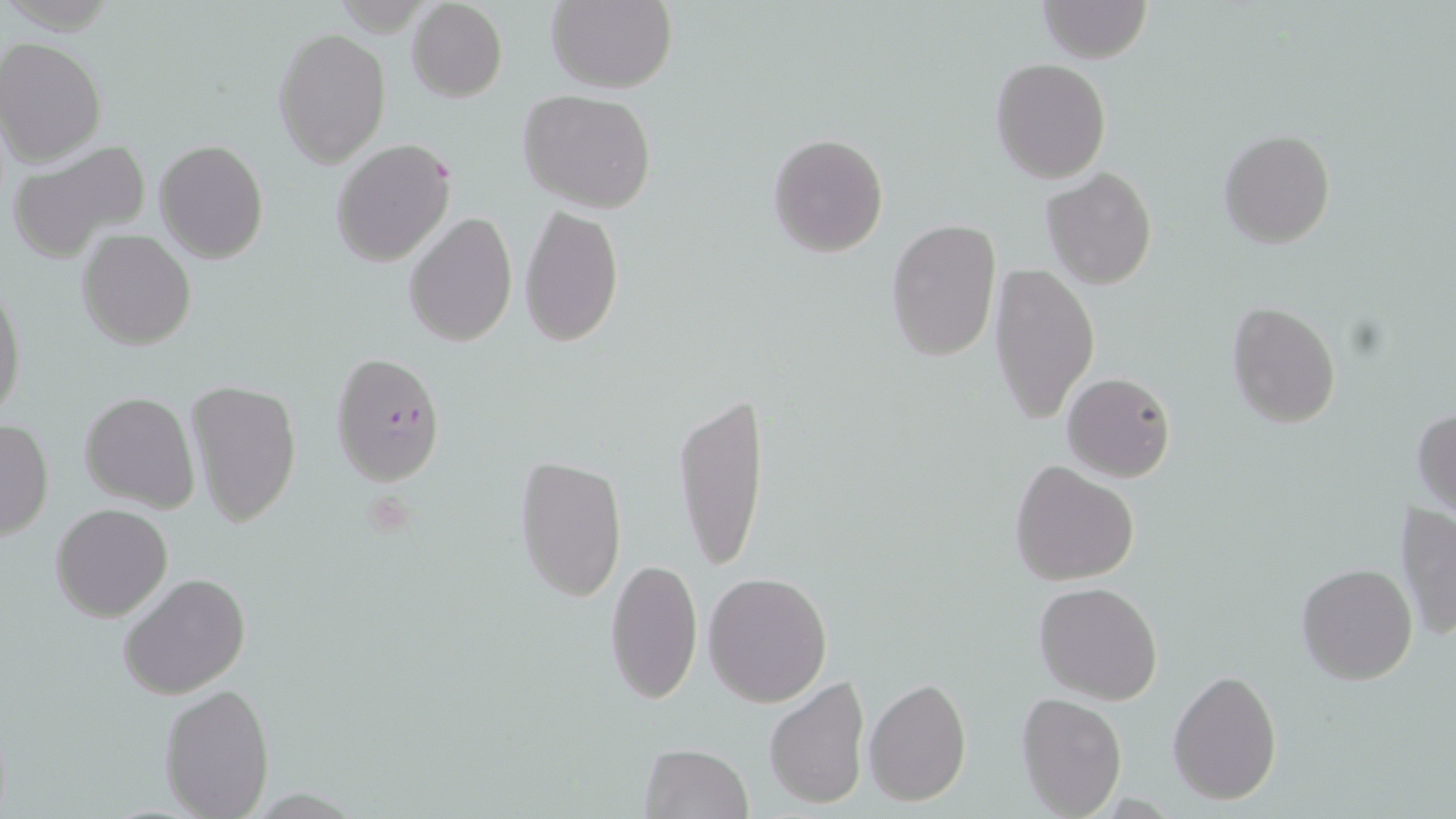
Summary:
  - Coordinate format: approximate bounding boxes as (x1, y1, x2, y2) in pixels
  - Uninfected red blood cell locations: (547, 0, 677, 93), (1038, 0, 1151, 63), (407, 1, 507, 102), (273, 27, 392, 168), (0, 38, 106, 165), (990, 58, 1112, 184), (519, 90, 658, 214), (1218, 129, 1336, 248), (769, 133, 889, 257), (7, 139, 152, 262), (154, 139, 268, 263), (330, 139, 456, 266), (1041, 167, 1158, 291), (519, 205, 625, 347), (404, 212, 517, 346), (884, 217, 1001, 365), (78, 228, 195, 350), (988, 262, 1100, 424), (0, 281, 26, 423), (1226, 300, 1341, 427), (1062, 372, 1176, 482), (185, 379, 303, 527), (79, 392, 199, 512), (674, 392, 769, 571), (1412, 406, 1456, 518), (0, 418, 55, 540), (514, 453, 627, 602), (1010, 460, 1138, 586), (1394, 500, 1456, 641), (51, 502, 173, 622), (603, 557, 704, 706), (1296, 562, 1419, 685), (704, 569, 833, 706), (119, 571, 251, 699), (1033, 581, 1163, 703), (1168, 669, 1282, 804), (764, 676, 870, 811), (864, 679, 971, 806), (157, 682, 277, 818), (1016, 693, 1128, 818), (638, 743, 755, 817)
  - Plasmodium falciparum-infected red blood cell locations: (330, 351, 445, 486)
  - Slide-level diagnosis: Plasmodium falciparum
  - Magnification: 1000x
  - Modality: optical microscopy
  - Image size: 1456×819 pixels
  - Field of view: one of a larger specimen
  - Stain: May-Grünwald-Giemsa
  - Preparation: thin blood smear